Outline each blood parasite and name the species.
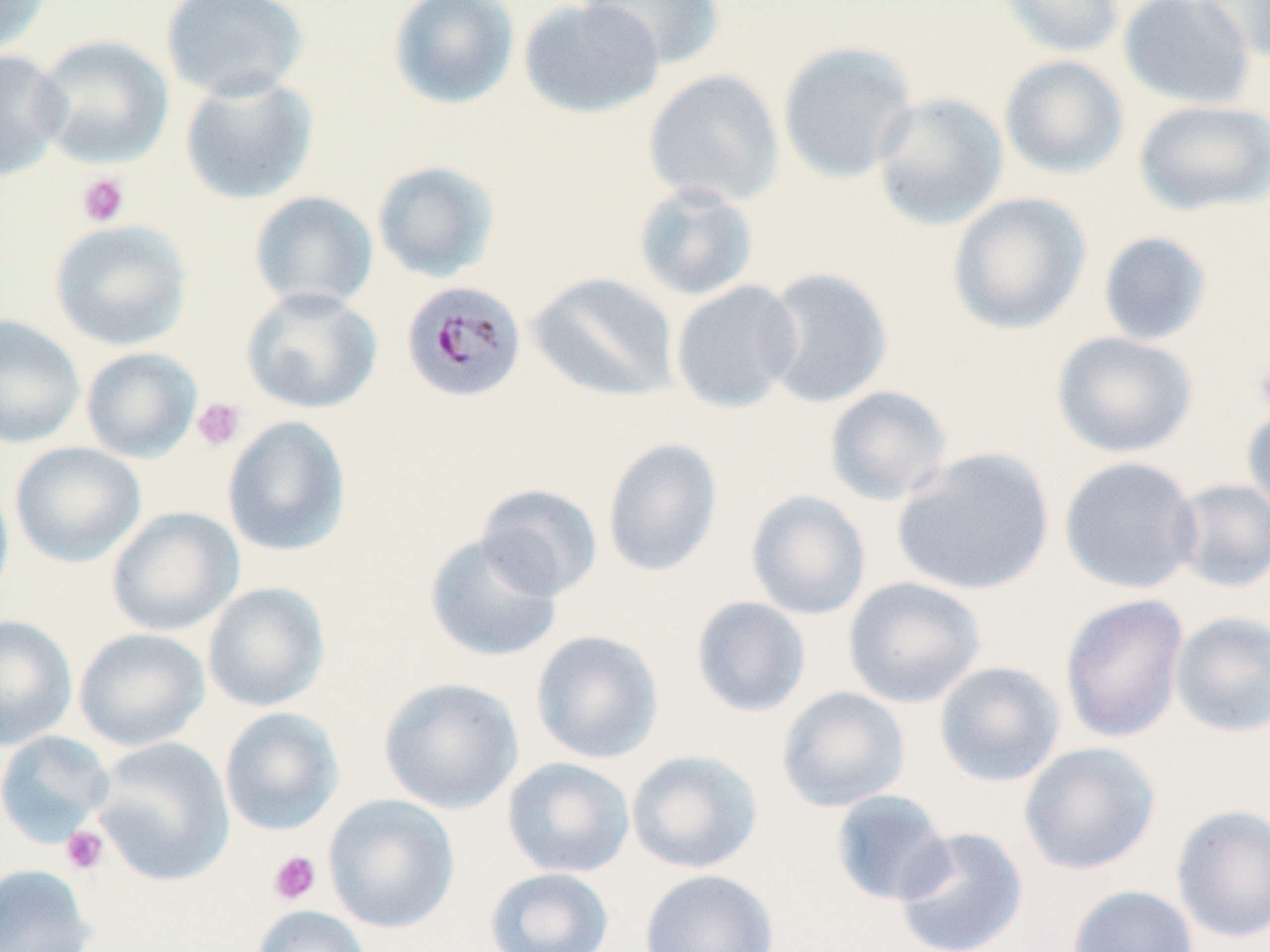

Approximate bounding boxes as [x1, y1, x2, y2] in pixels.
Plasmodium malariae-infected red blood cells: [400, 279, 527, 403].
No Plasmodium falciparum, Plasmodium ovale, Plasmodium vivax, Babesia divergens, or Trypanosoma brucei observed.

slide_level_diagnosis: Plasmodium malariae
magnification: 1000x
image_size: 1270×952 pixels
preparation: thin blood film
field_of_view: one of a larger specimen
modality: light microscopy
stain: May-Grünwald-Giemsa
platelet_locations: 'approximate bounding boxes as [x1, y1, x2, y2] in pixels: [76, 173, 129, 227], [1252, 360, 1270, 416], [191, 397, 246, 452], [61, 825, 109, 875], [268, 851, 321, 905]'
uninfected_red_blood_cell_locations: 'approximate bounding boxes as [x1, y1, x2, y2] in pixels: [0, 0, 52, 55], [160, 0, 310, 102], [387, 0, 520, 110], [517, 0, 665, 119], [580, 0, 727, 70], [995, 0, 1127, 58], [1118, 0, 1256, 110], [1192, 0, 1270, 61], [31, 34, 174, 168], [777, 40, 919, 185], [0, 48, 69, 182], [999, 54, 1129, 180], [643, 69, 785, 207], [179, 72, 319, 205], [870, 91, 1009, 231], [1133, 98, 1270, 217], [371, 160, 500, 283], [632, 180, 760, 302], [248, 190, 378, 312], [947, 191, 1092, 335], [48, 218, 192, 351], [1097, 231, 1213, 347], [759, 267, 894, 409], [527, 272, 680, 403], [670, 279, 803, 413], [240, 286, 382, 414], [0, 314, 85, 449], [1051, 331, 1199, 459], [80, 346, 202, 463], [824, 385, 952, 506], [1241, 401, 1270, 525], [222, 415, 351, 557], [602, 437, 723, 577], [9, 442, 146, 567], [891, 446, 1055, 597], [1059, 455, 1202, 595], [0, 471, 15, 610], [1170, 478, 1270, 593], [476, 484, 603, 601], [746, 490, 871, 620], [106, 506, 244, 636], [424, 532, 563, 663], [842, 576, 986, 709], [202, 582, 330, 712], [1059, 593, 1189, 745], [690, 596, 812, 717], [1169, 611, 1270, 738], [0, 615, 78, 750], [73, 627, 211, 752], [530, 629, 664, 764], [933, 660, 1066, 787], [378, 676, 523, 814], [777, 685, 911, 813], [219, 707, 345, 836], [0, 730, 115, 847], [91, 737, 235, 886], [1018, 741, 1161, 875], [625, 749, 763, 874], [502, 757, 636, 878], [830, 789, 954, 906], [323, 794, 459, 933], [1170, 803, 1270, 944], [893, 826, 1029, 952], [0, 863, 97, 952], [485, 867, 615, 952], [639, 868, 779, 952], [1067, 885, 1200, 952], [251, 904, 370, 952]'